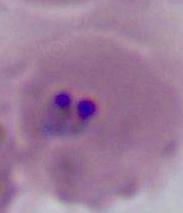
identification = Plasmodium
modality = micrograph
magnification = 400x or 1000x